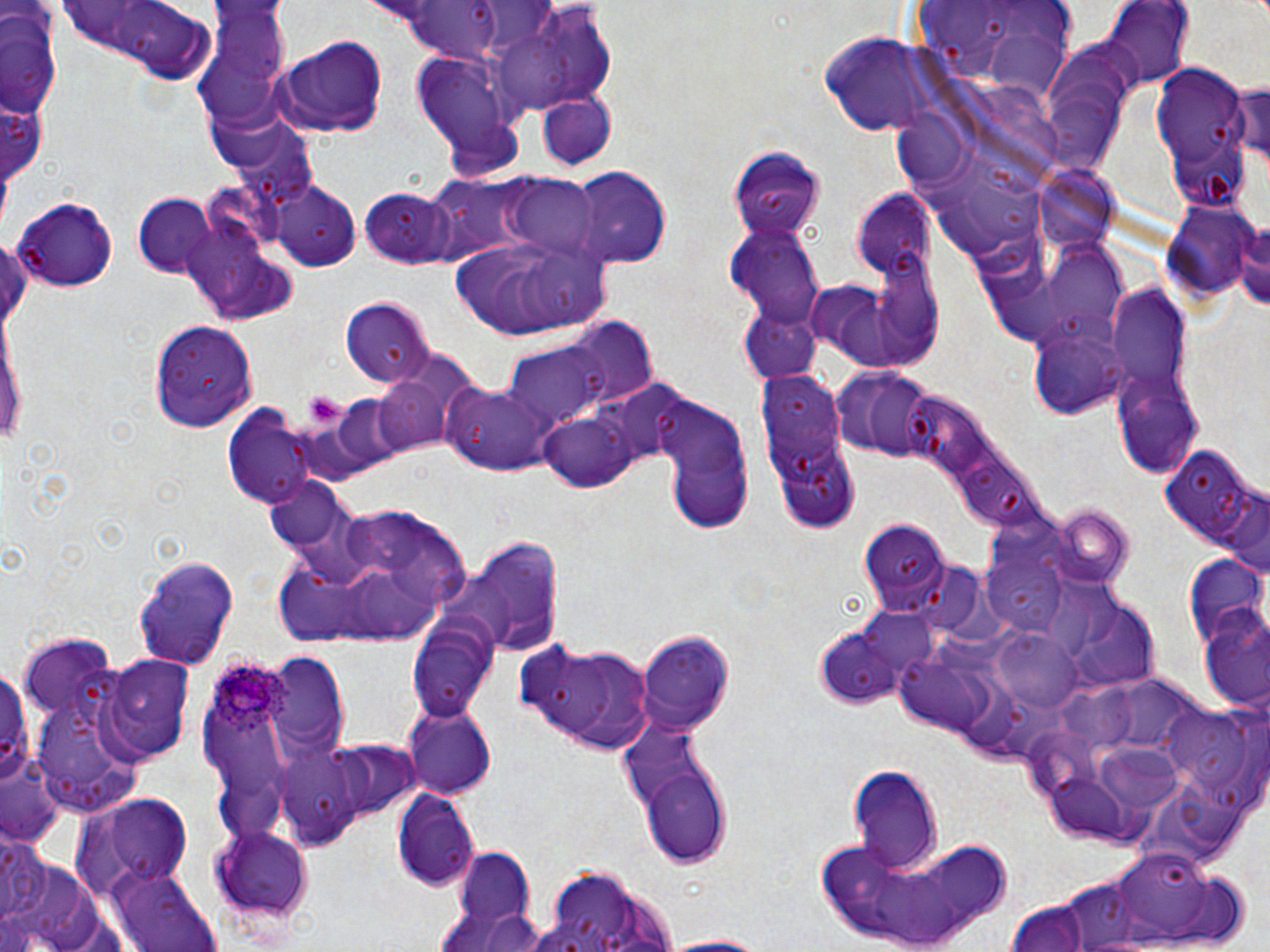

slide-level diagnosis = Plasmodium ovale
platelet locations = approximate bounding boxes as (x1,y1)-(x2,y2) corner pairs in pixels: (304,390)-(345,429)
magnification = 1000x
image size = 1270×952 pixels
preparation = thin blood smear
modality = optical microscopy
field of view = one of a larger specimen
stain = May-Grünwald-Giemsa
Plasmodium ovale-infected red blood cell locations = approximate bounding boxes as (x1,y1)-(x2,y2) corner pairs in pixels: (211,658)-(292,740)
uninfected red blood cell locations = approximate bounding boxes as (x1,y1)-(x2,y2) corner pairs in pixels: (57,0)-(217,78), (1106,3)-(1195,89), (197,8)-(295,138), (490,8)-(614,112), (1,12)-(64,122), (817,29)-(945,133), (270,34)-(390,140), (1039,41)-(1139,171), (413,51)-(521,161), (1152,67)-(1249,182), (1234,76)-(1270,168), (206,91)-(294,173), (537,92)-(616,169), (1,94)-(45,185), (890,101)-(976,191), (729,143)-(825,242), (1038,163)-(1119,253), (566,165)-(674,268), (421,178)-(521,265), (506,178)-(599,255), (271,181)-(361,270), (357,186)-(462,270), (851,191)-(939,279), (132,194)-(218,277), (13,195)-(117,293), (1164,200)-(1261,303), (1236,212)-(1270,316), (182,218)-(300,323), (724,223)-(823,324), (447,231)-(616,339), (1047,242)-(1134,343), (856,246)-(948,372), (1105,290)-(1195,398), (339,296)-(434,387), (739,304)-(822,384), (0,313)-(26,454), (151,318)-(255,432), (1027,320)-(1131,420), (500,333)-(624,434), (835,364)-(940,464), (371,366)-(460,456), (758,367)-(863,531), (1112,371)-(1204,477), (442,380)-(561,478), (331,395)-(412,473), (654,396)-(755,530), (541,407)-(645,492), (222,409)-(318,506), (1160,441)-(1263,562), (263,476)-(358,557), (1223,492)-(1270,582), (1048,505)-(1134,591), (855,519)-(953,611), (380,526)-(472,608), (443,535)-(566,656), (981,551)-(1065,635), (1182,554)-(1266,648), (133,555)-(241,669), (279,558)-(350,644), (1067,602)-(1162,690), (816,606)-(944,709), (1200,613)-(1270,710), (405,614)-(502,723), (637,631)-(735,735), (998,634)-(1087,715), (20,635)-(112,723), (517,639)-(654,753), (268,655)-(345,753), (99,656)-(195,760), (0,660)-(35,788), (897,661)-(981,737), (1167,703)-(1268,813), (400,704)-(498,798), (270,739)-(383,845), (333,740)-(420,821), (1096,743)-(1191,811), (0,761)-(64,847), (641,764)-(734,867), (849,766)-(943,872), (1044,773)-(1136,846), (391,786)-(482,893), (70,795)-(195,896), (211,827)-(314,923), (812,827)-(1012,952), (1,835)-(50,924), (447,843)-(539,944), (1109,847)-(1226,943), (0,854)-(114,951), (109,865)-(220,952), (550,868)-(626,936), (1064,878)-(1139,946), (1003,903)-(1094,952), (651,934)-(773,951)